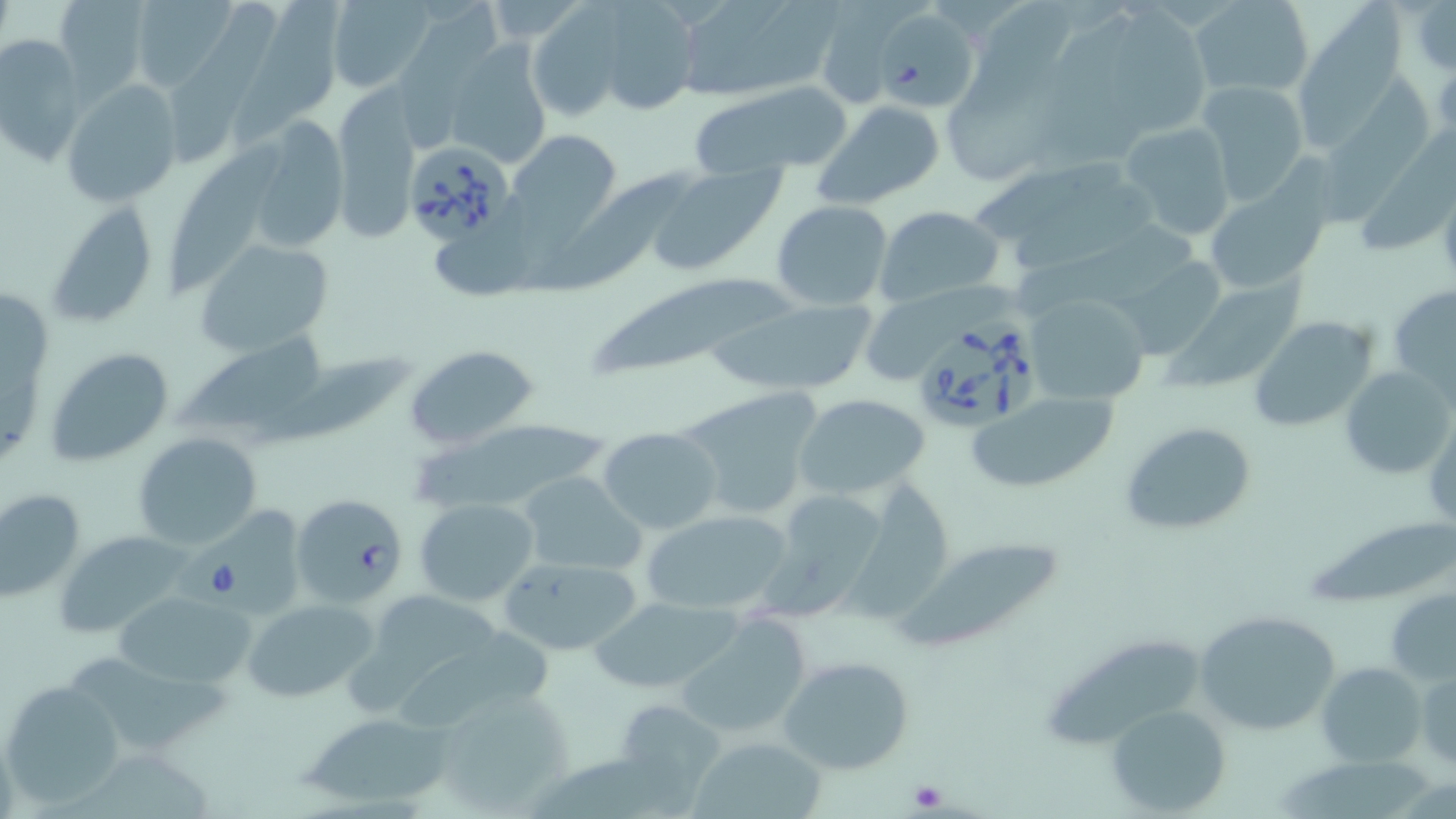 Approximate bounding boxes as [x1, y1, x2, y2] in pixels. Uninfected red blood cell locations: [54, 0, 152, 99], [128, 0, 239, 93], [229, 0, 340, 151], [325, 0, 436, 92], [1403, 0, 1456, 74], [671, 1, 835, 101], [1188, 1, 1315, 96], [164, 2, 278, 164], [587, 2, 702, 118], [809, 3, 913, 111], [526, 5, 625, 121], [974, 5, 1076, 97], [1116, 5, 1218, 139], [871, 7, 979, 114], [1045, 13, 1145, 166], [1, 33, 88, 165], [445, 42, 551, 168], [941, 72, 1060, 184], [1318, 72, 1434, 231], [63, 80, 182, 207], [688, 80, 857, 181], [1196, 81, 1311, 207], [333, 93, 419, 241], [813, 101, 946, 207], [241, 117, 352, 255], [1118, 121, 1237, 242], [1358, 126, 1456, 256], [510, 130, 622, 234], [164, 140, 285, 298], [649, 164, 786, 275], [530, 166, 691, 294], [1203, 182, 1325, 293], [1012, 186, 1166, 266], [46, 200, 159, 331], [771, 201, 893, 310], [873, 205, 1004, 307], [1008, 222, 1199, 301], [432, 229, 536, 304], [194, 238, 335, 356], [1112, 257, 1223, 361], [1158, 271, 1309, 390], [592, 279, 800, 380], [1390, 283, 1456, 400], [864, 284, 1021, 386], [1024, 290, 1150, 405], [706, 296, 878, 396], [1249, 316, 1380, 432], [179, 331, 327, 433], [405, 344, 539, 451], [44, 347, 174, 467], [255, 357, 414, 451], [1342, 364, 1453, 480], [676, 389, 825, 522], [967, 391, 1120, 494], [793, 394, 931, 499], [1120, 421, 1258, 536], [403, 423, 609, 513], [598, 427, 723, 534], [134, 432, 263, 550], [516, 472, 648, 576], [839, 475, 952, 624], [0, 487, 87, 601], [766, 488, 892, 615], [414, 498, 540, 605], [640, 508, 794, 616], [1313, 513, 1456, 607], [57, 531, 195, 639], [892, 533, 1073, 654], [497, 555, 641, 655], [1385, 585, 1456, 686], [113, 590, 256, 689], [343, 594, 494, 718], [590, 595, 743, 696], [244, 598, 376, 702], [674, 610, 820, 740], [1193, 610, 1339, 735], [403, 624, 557, 727], [1043, 634, 1201, 752], [75, 645, 235, 752], [777, 654, 915, 774], [1317, 662, 1425, 767], [1415, 662, 1456, 771], [2, 681, 122, 807], [428, 686, 573, 815], [623, 701, 727, 815], [1107, 707, 1231, 817], [300, 712, 455, 809], [691, 733, 829, 819], [1278, 753, 1434, 819]. Platelet locations: [197, 558, 245, 600], [905, 776, 952, 813]. Babesia divergens-infected red blood cell locations: [402, 138, 517, 245], [915, 318, 1038, 433], [290, 494, 406, 603]. Slide-level diagnosis: Babesia divergens. One field of a larger specimen. May-Grünwald-Giemsa stain. 1000x magnification. Image is 1456×819 pixels. Light microscopy. Thin blood film.